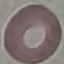

Summary:
  - Malaria status: uninfected
  - Capture: smartphone camera at the microscope eyepiece
  - Preparation: thin blood film
  - Stain: Giemsa
  - Image type: automatically extracted cell patch, resized to 64 × 64 pixels